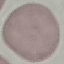
Malaria status: uninfected. Photographed with a smartphone camera at the microscope eyepiece. Automatically extracted cell patch, resized to 64 × 64 pixels. Thin smear of blood. Giemsa-stained preparation.